Describe the morphology of the erythrocytes.
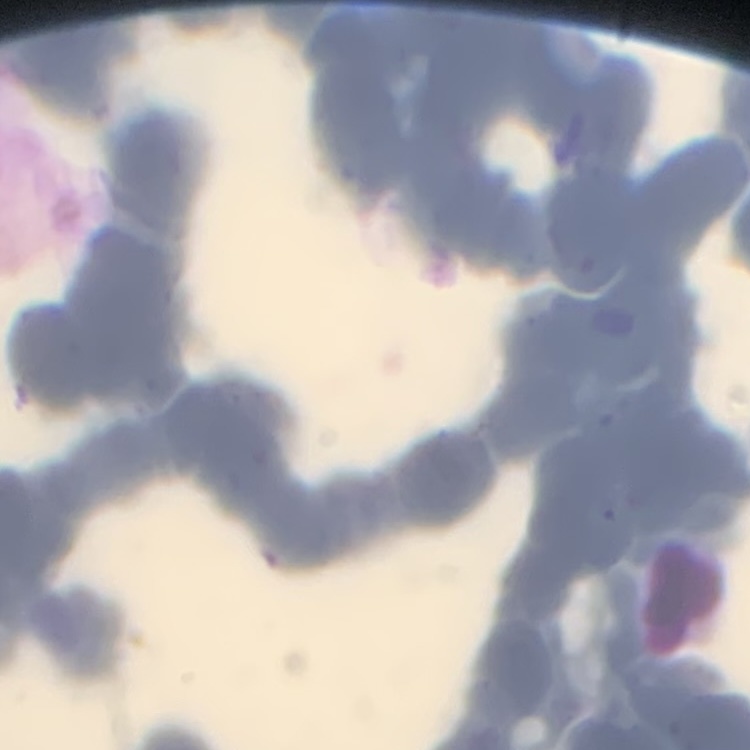

Rouleaux formation.

Summary:
  - Image type: square crop of a larger photomicrograph
  - Preparation: thin peripheral smear
  - Stain: Field's or Giemsa